Outline each blood parasite and name the species.
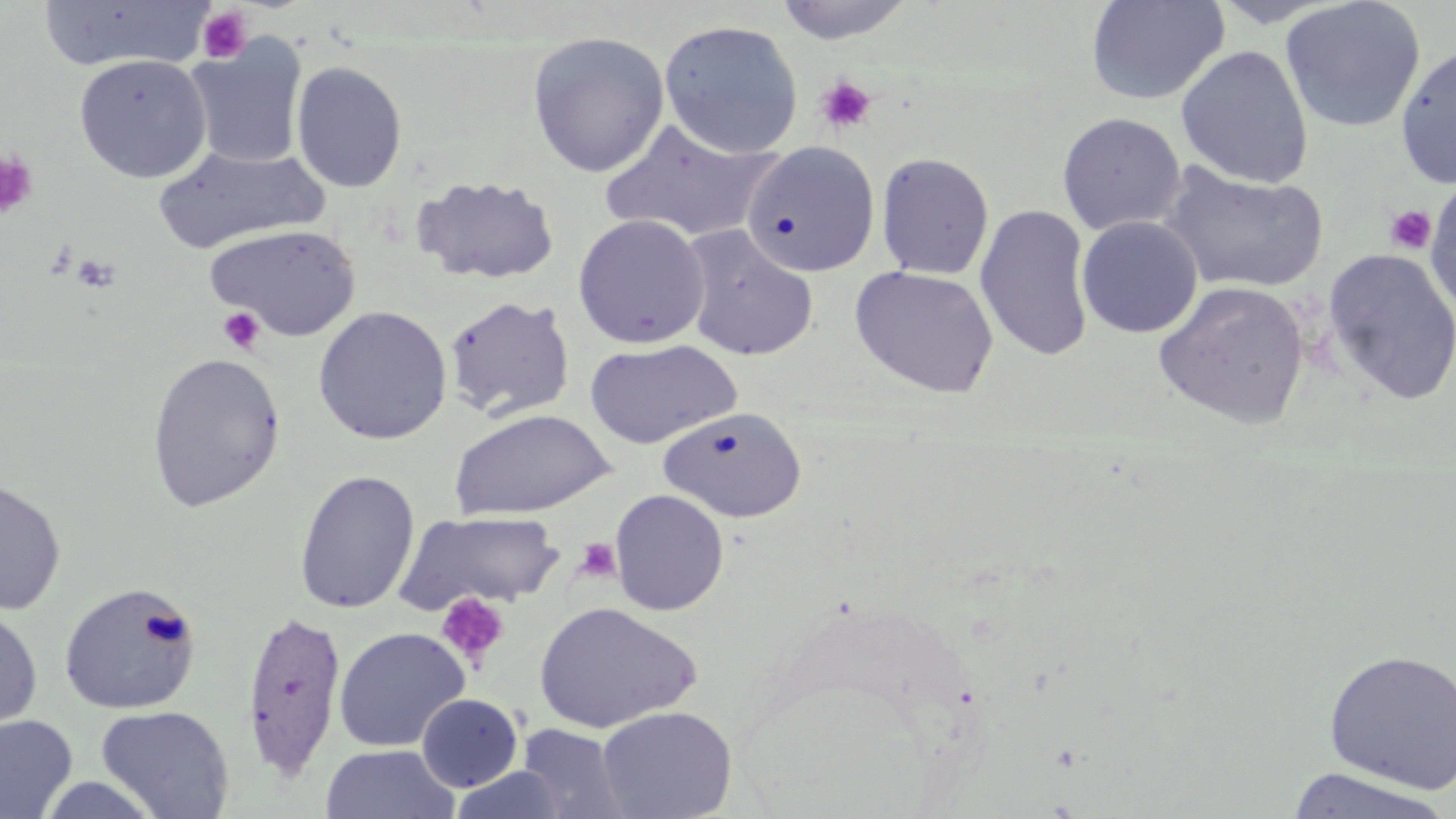
No blood parasites observed.

{
  "slide_level_diagnosis": "no evidence of blood parasites",
  "platelet_locations": "approximate bounding boxes as (x1,y1)-(x2,y2) corner pairs in pixels: (196,7)-(253,63), (815,74)-(877,135), (0,151)-(38,220), (1383,205)-(1437,255), (72,254)-(120,293), (217,306)-(266,354), (574,537)-(622,584), (434,592)-(510,669)",
  "uninfected_red_blood_cell_locations": "approximate bounding boxes as (x1,y1)-(x2,y2) corner pairs in pixels: (1085,0)-(1231,106), (1280,0)-(1426,133), (36,1)-(213,73), (771,1)-(918,45), (658,20)-(804,158), (527,31)-(669,178), (185,37)-(307,170), (1395,42)-(1456,188), (1175,45)-(1314,189), (74,54)-(212,183), (291,61)-(408,193), (1057,112)-(1186,235), (599,119)-(780,243), (741,143)-(880,278), (153,145)-(329,254), (875,151)-(994,280), (1160,163)-(1329,295), (1423,174)-(1456,320), (411,175)-(560,285), (975,204)-(1094,363), (572,214)-(710,349), (1077,216)-(1202,338), (205,224)-(361,341), (680,226)-(819,362), (1321,248)-(1456,405), (849,265)-(999,399), (1152,280)-(1310,429), (444,295)-(576,423), (313,306)-(452,444), (584,339)-(741,449), (146,353)-(285,513), (658,406)-(806,523), (448,409)-(615,520), (294,469)-(420,614), (0,479)-(66,616), (608,489)-(729,616), (396,509)-(565,613), (58,581)-(201,715), (532,601)-(701,733), (0,607)-(42,735), (240,609)-(347,782), (333,627)-(470,752), (1323,648)-(1456,794), (417,693)-(523,792), (96,705)-(234,818), (596,705)-(737,818), (0,714)-(78,819), (515,723)-(631,818), (320,744)-(460,819), (1285,766)-(1452,818), (36,774)-(166,818)",
  "modality": "optical microscopy",
  "preparation": "thin blood smear",
  "stain": "May-Grünwald-Giemsa",
  "image_size": "1456×819 pixels",
  "magnification": "1000x",
  "field_of_view": "one of a larger specimen"
}